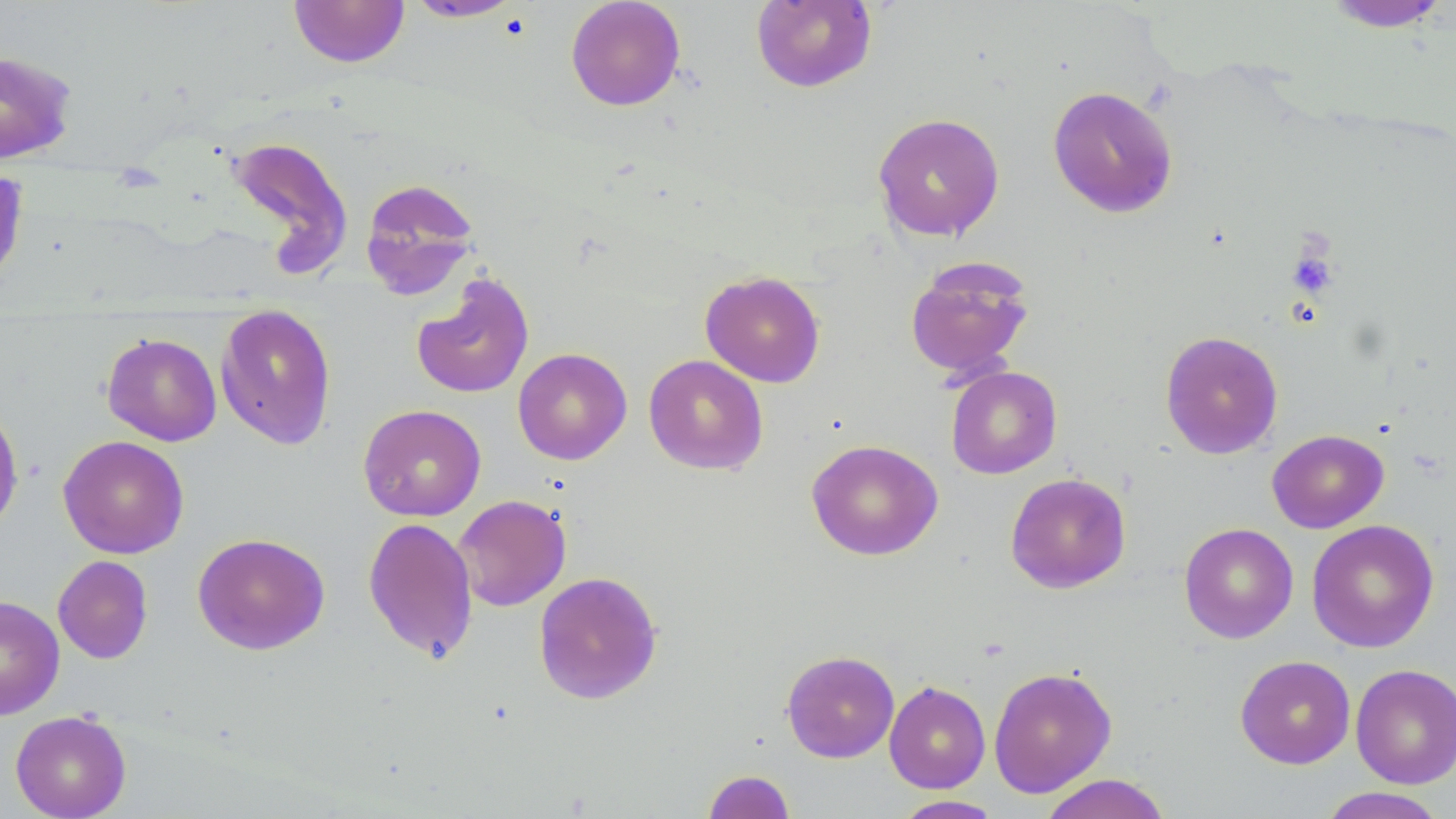
slide-level diagnosis = no evidence of blood parasites
magnification = 1000x
stain = May-Grünwald-Giemsa
image size = 1456×819 pixels
uninfected red blood cell locations = approximate bounding boxes as (x1, y1, x2, y2) in pixels: (565, 0, 686, 111), (288, 1, 410, 68), (403, 1, 524, 23), (751, 1, 877, 92), (1320, 1, 1452, 32), (0, 49, 78, 164), (1047, 86, 1179, 218), (872, 113, 1005, 242), (222, 134, 354, 277), (0, 167, 31, 293), (359, 177, 481, 299), (904, 258, 1036, 382), (700, 270, 826, 388), (410, 272, 535, 400), (215, 303, 337, 450), (1160, 330, 1284, 459), (101, 333, 222, 446), (513, 347, 632, 465), (643, 354, 768, 476), (946, 365, 1062, 479), (0, 401, 24, 535), (358, 404, 486, 521), (1267, 429, 1389, 533), (58, 435, 189, 559), (806, 439, 943, 561), (1005, 472, 1131, 593), (453, 494, 571, 611), (362, 516, 478, 663), (1307, 518, 1439, 653), (1179, 522, 1299, 644), (192, 532, 330, 655), (52, 555, 153, 664), (533, 571, 663, 705), (0, 595, 65, 721), (781, 649, 900, 763), (1235, 655, 1356, 769), (1351, 664, 1456, 789), (988, 666, 1117, 797), (884, 680, 991, 793), (10, 710, 131, 819), (702, 769, 796, 819), (1038, 773, 1172, 819), (1315, 787, 1450, 818), (892, 795, 1004, 818)
preparation = thin blood smear
field of view = one of a larger specimen
modality = light microscopy
platelet locations = approximate bounding boxes as (x1, y1, x2, y2) in pixels: (1288, 248, 1337, 297)